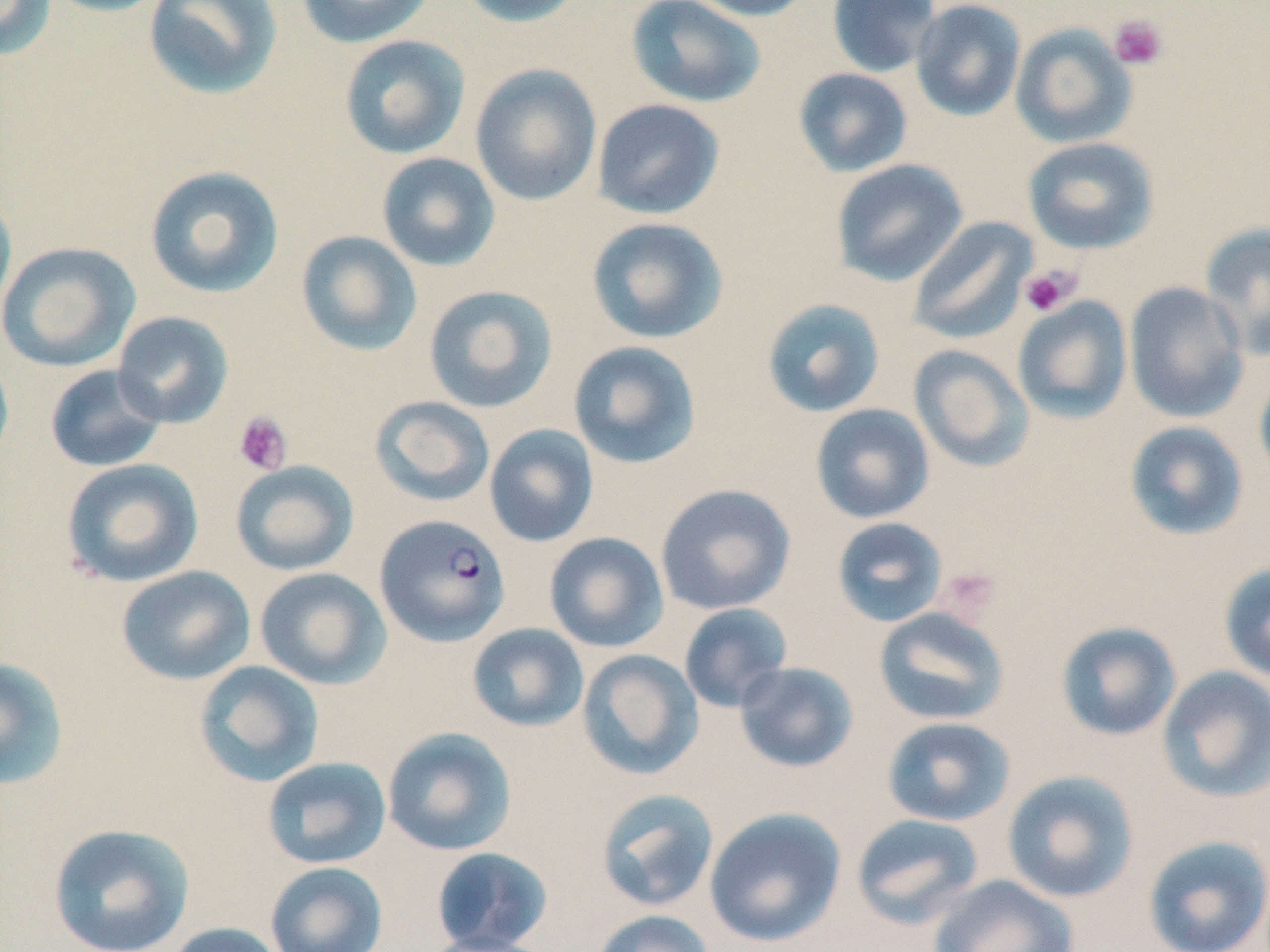

Summary:
  - Coordinate format: approximate bounding boxes as [x1, y1, x2, y2] in pixels
  - Plasmodium falciparum-infected red blood cell locations: [375, 513, 511, 646]
  - Platelet locations: [1107, 14, 1168, 71], [1019, 264, 1081, 317], [233, 411, 292, 475], [936, 566, 1001, 621]
  - Uninfected red blood cell locations: [0, 0, 58, 60], [41, 0, 173, 17], [142, 0, 284, 101], [295, 0, 436, 48], [456, 0, 586, 28], [682, 0, 817, 22], [827, 0, 941, 77], [910, 0, 1026, 121], [626, 1, 766, 108], [1010, 23, 1137, 148], [338, 34, 471, 159], [470, 64, 603, 206], [793, 68, 913, 177], [592, 98, 725, 219], [1022, 136, 1159, 255], [376, 152, 501, 272], [831, 159, 968, 286], [144, 165, 285, 298], [0, 191, 17, 325], [586, 217, 729, 345], [906, 217, 1037, 345], [1199, 221, 1270, 360], [295, 230, 422, 357], [0, 241, 140, 372], [1124, 282, 1250, 423], [423, 284, 558, 413], [1012, 296, 1132, 423], [762, 298, 886, 418], [112, 311, 234, 429], [568, 340, 702, 469], [909, 344, 1035, 472], [0, 349, 15, 472], [44, 364, 167, 472], [1254, 367, 1270, 485], [369, 395, 495, 507], [810, 403, 935, 524], [1124, 421, 1249, 541], [483, 424, 600, 548], [60, 457, 204, 588], [230, 460, 359, 576], [655, 484, 796, 615], [832, 516, 948, 628], [543, 532, 669, 652], [1219, 561, 1270, 684], [116, 565, 256, 686], [253, 566, 392, 690], [678, 603, 793, 712], [873, 607, 1009, 726], [1055, 621, 1182, 742], [467, 623, 589, 732], [577, 649, 704, 780], [0, 656, 70, 791], [193, 660, 324, 788], [734, 661, 860, 773], [1156, 666, 1270, 802], [881, 716, 1016, 827], [381, 726, 517, 856], [261, 756, 392, 870], [1001, 770, 1139, 904], [595, 788, 720, 913], [704, 806, 846, 947], [850, 813, 985, 929], [46, 822, 196, 952], [1142, 835, 1270, 952], [430, 847, 554, 952], [265, 861, 388, 952], [927, 874, 1079, 952], [590, 909, 716, 952], [162, 921, 289, 952], [418, 932, 558, 952]
  - Slide-level diagnosis: Plasmodium falciparum
  - Field of view: single
  - Modality: light microscopy
  - Image size: 1270×952 pixels
  - Magnification: 1000x
  - Stain: May-Grünwald-Giemsa
  - Preparation: thin blood smear